Classify this cell by malaria status.
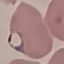

It is parasitized.

Summary:
  - Image type: automatically extracted cell patch, resized to 64 × 64 pixels
  - Stain: Giemsa
  - Capture: smartphone through the microscope eyepiece
  - Preparation: thin blood smear